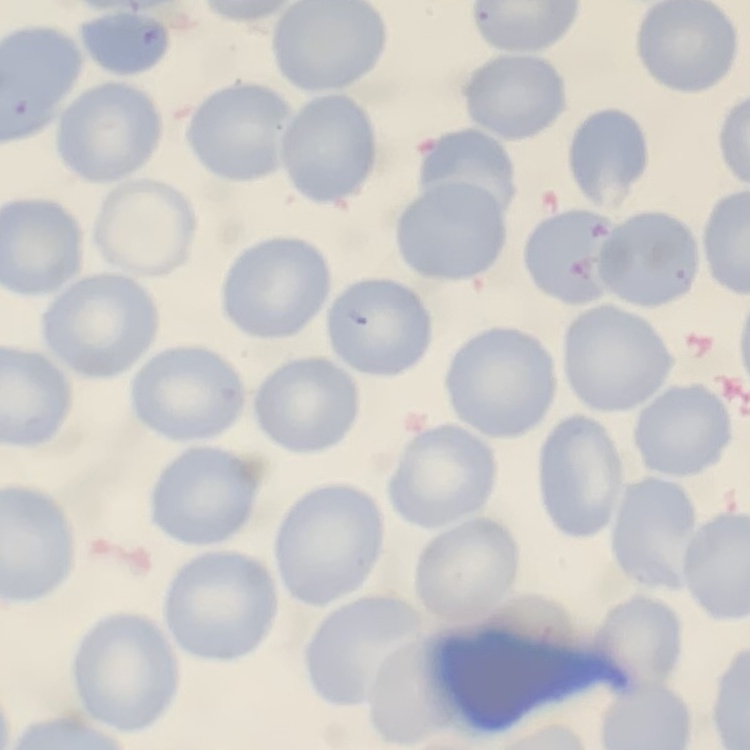

The red blood cells exhibit no rouleaux formation. Square crop of a larger photomicrograph. Thin blood smear. Field's or Giemsa stain.